Assess this cell for malaria.
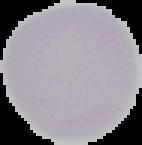

It is uninfected.

Summary:
  - Image size: 142×145 pixels
  - Preparation: thin blood smear
  - Image type: segmented cell region with the area outside set to black